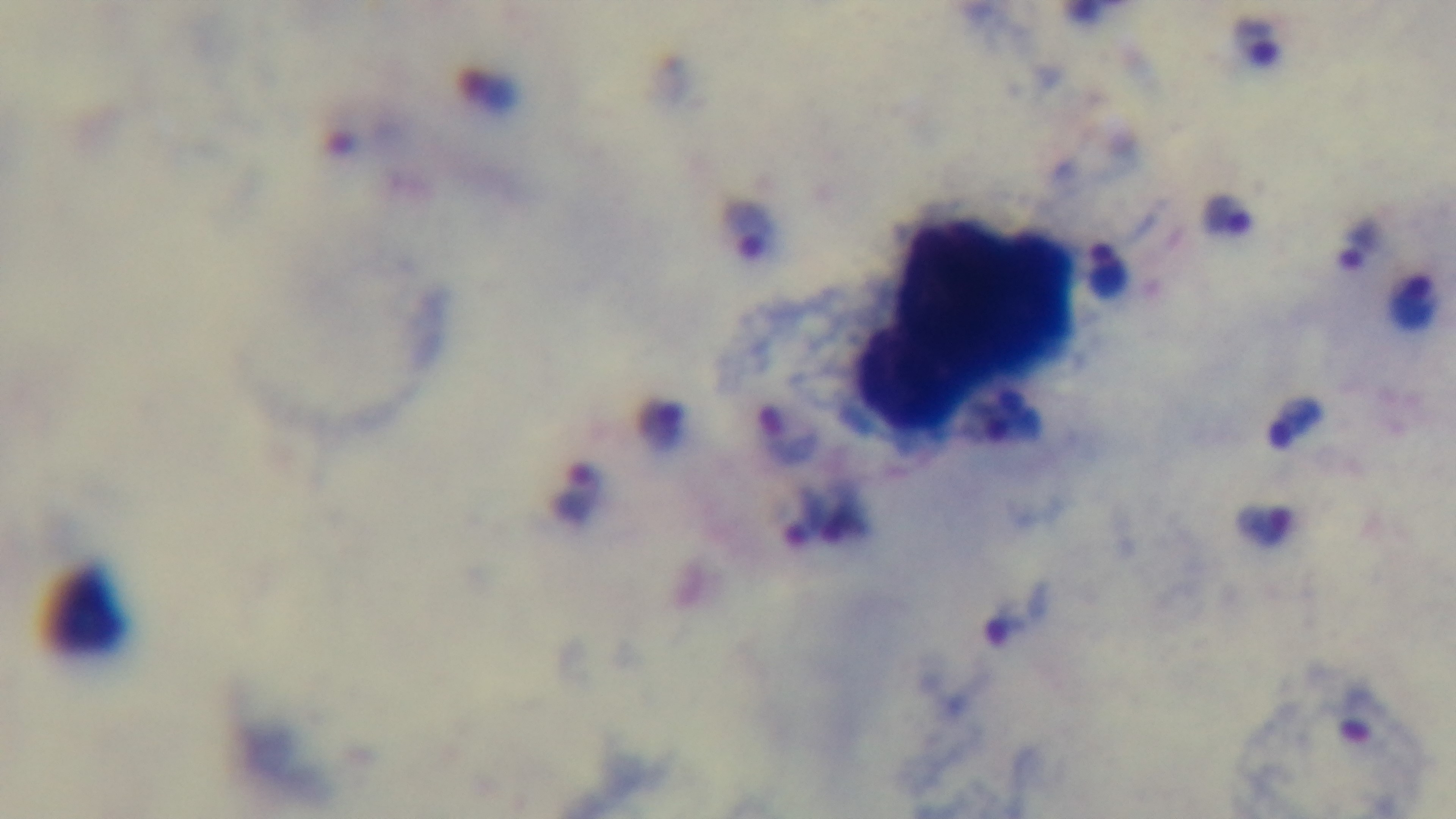
objective: 100x oil immersion
field_of_view: single
preparation: thick smear
malaria_status: infected
capture: mounted 4K digital camera
stain: Giemsa
modality: light microscopy